Locate every leukocyte (white blood cell).
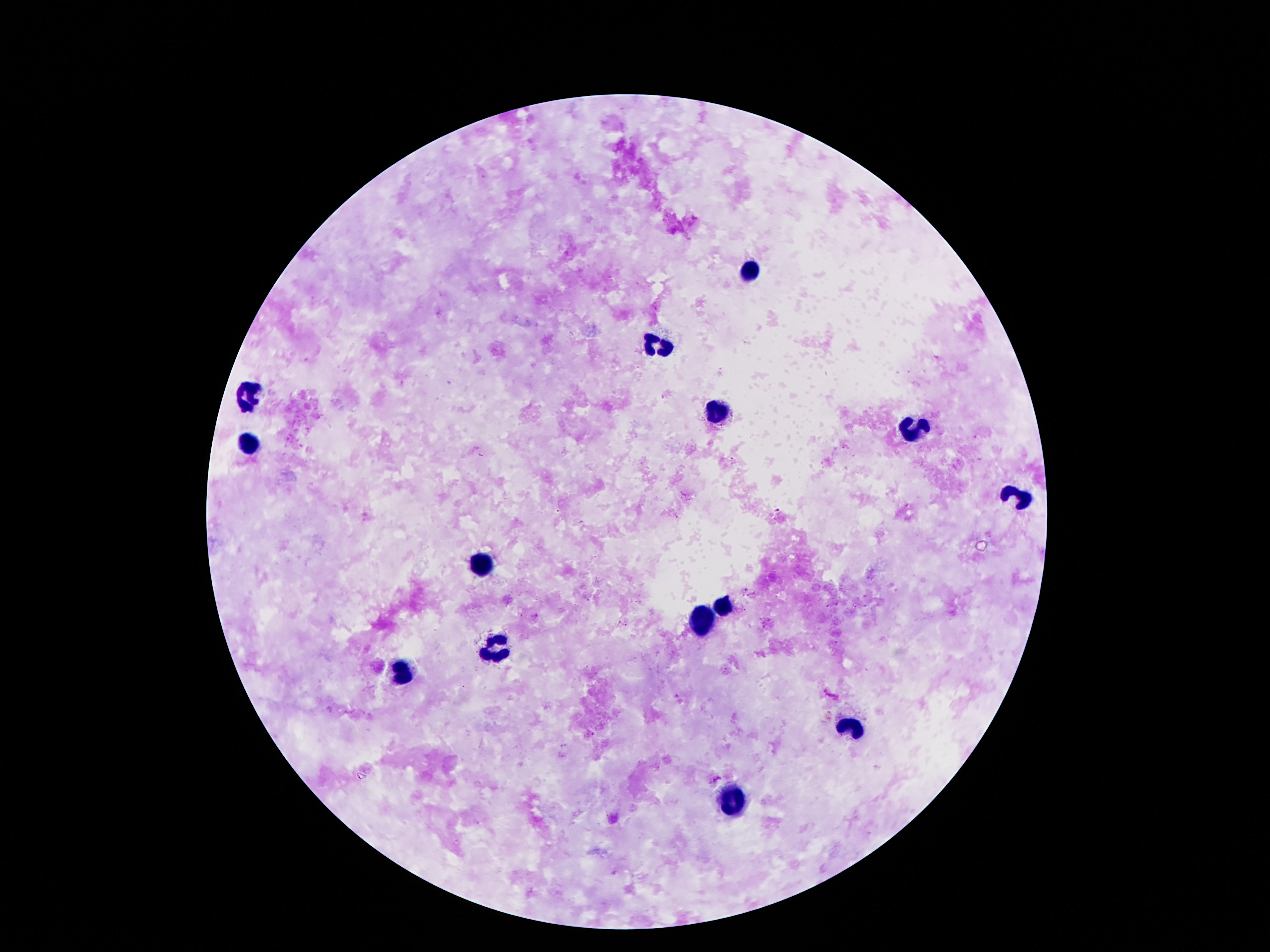
Approximate centers as [x, y] in pixels.
Leukocytes: [749, 270], [662, 343], [247, 397], [716, 413], [914, 429], [247, 448], [1015, 497], [482, 565], [721, 604], [700, 622], [496, 646], [398, 672], [851, 726], [730, 803].

Thick blood smear. Giemsa stain. Patient malaria status: negative. 100x magnification. One field from this slide. Smartphone photograph taken through the microscope eyepiece. Image is 1270×952 pixels.